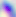
Captured at 400x magnification. Micrograph. Toxoplasma gondii is seen.